Outline each Plasmodium vivax-infected red blood cell.
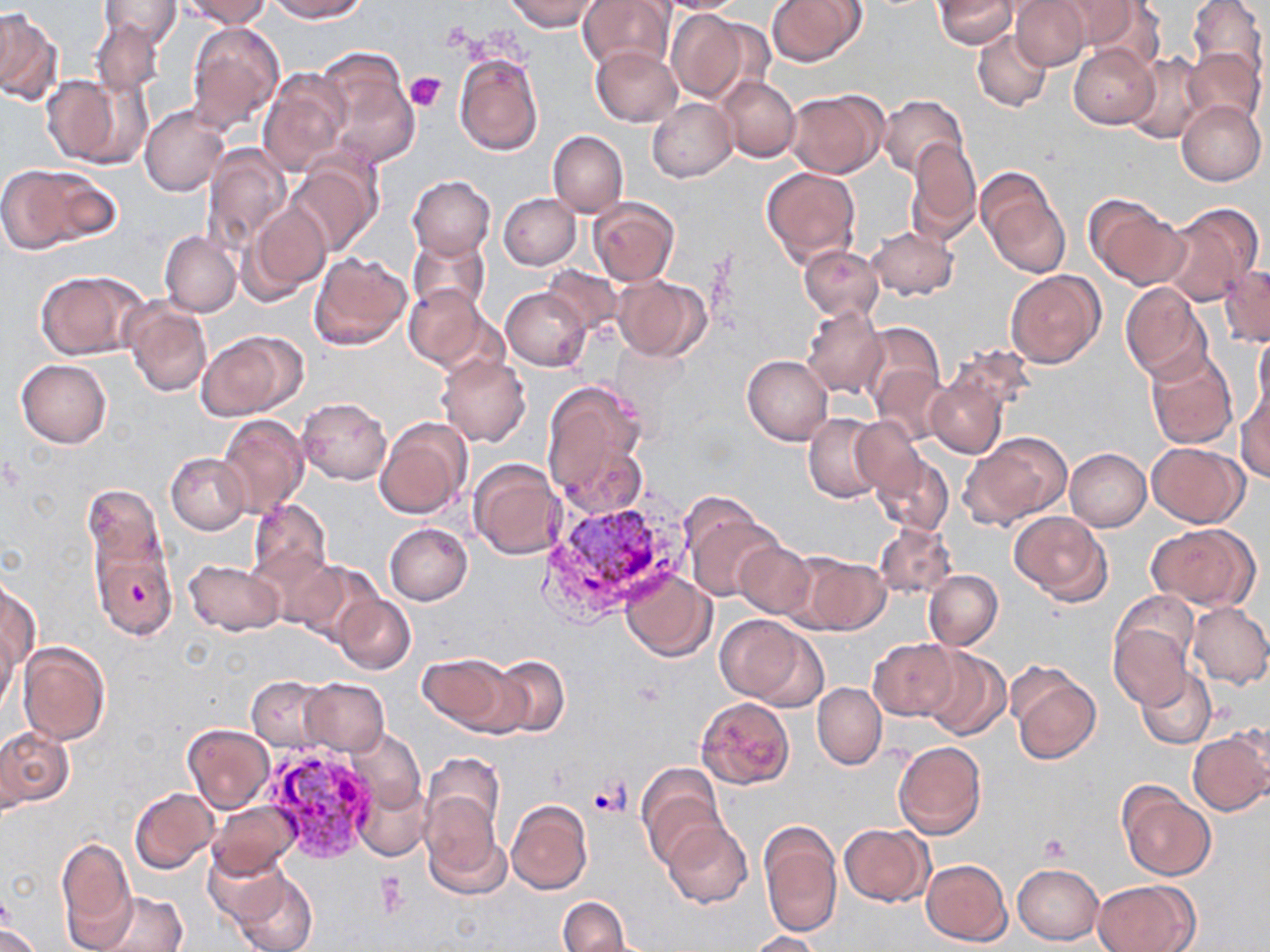

Approximate bounding boxes as (x1, y1, x2, y2) in pixels.
Plasmodium vivax-infected red blood cells: (543, 499, 678, 588), (255, 741, 375, 863).

Uninfected red blood cell locations: (99, 0, 181, 48), (177, 0, 274, 27), (266, 0, 366, 22), (504, 0, 600, 33), (579, 0, 676, 73), (652, 0, 752, 14), (766, 0, 866, 67), (934, 0, 1018, 49), (1010, 0, 1092, 70), (1052, 0, 1151, 54), (1186, 0, 1267, 81), (1019, 2, 1158, 84), (0, 8, 62, 105), (666, 8, 761, 104), (91, 17, 165, 98), (186, 21, 285, 134), (972, 30, 1052, 112), (1069, 43, 1160, 128), (591, 46, 683, 127), (1184, 48, 1265, 128), (454, 51, 544, 156), (1123, 52, 1209, 144), (314, 55, 420, 173), (260, 68, 352, 175), (40, 73, 132, 168), (715, 76, 800, 162), (784, 88, 886, 178), (879, 95, 968, 180), (647, 99, 737, 182), (1176, 100, 1266, 185), (140, 105, 231, 197), (548, 130, 628, 217), (905, 138, 981, 243), (201, 143, 293, 252), (286, 157, 382, 255), (1, 162, 118, 253), (762, 166, 861, 270), (978, 171, 1068, 276), (408, 176, 495, 259), (498, 194, 581, 270), (1086, 195, 1190, 289), (588, 197, 678, 287), (240, 203, 329, 304), (1159, 203, 1263, 304), (868, 227, 958, 299), (160, 232, 241, 317), (408, 232, 491, 316), (800, 246, 883, 321), (308, 250, 412, 351), (1219, 264, 1269, 346), (541, 266, 623, 334), (34, 270, 146, 360), (1006, 270, 1106, 370), (612, 275, 710, 360), (1120, 282, 1212, 382), (403, 284, 490, 371), (501, 287, 591, 370), (122, 300, 212, 398), (802, 304, 886, 399), (860, 321, 944, 412), (1254, 329, 1270, 421), (197, 331, 300, 421), (948, 347, 1034, 423), (1145, 348, 1239, 450), (743, 355, 833, 445), (438, 356, 530, 446), (16, 359, 111, 447), (872, 365, 951, 444), (926, 370, 1009, 459), (541, 379, 650, 512), (1236, 388, 1270, 483), (297, 398, 391, 485), (803, 412, 886, 503), (218, 414, 309, 517), (850, 416, 924, 497), (374, 417, 470, 520), (959, 431, 1072, 530), (1147, 442, 1247, 527), (1064, 448, 1150, 530), (870, 450, 955, 537), (166, 452, 250, 534), (467, 459, 564, 561), (82, 485, 169, 584), (683, 494, 781, 592), (248, 498, 333, 595), (1009, 511, 1110, 602), (873, 522, 956, 598), (384, 523, 474, 605), (1146, 524, 1259, 611), (89, 527, 175, 642), (734, 542, 814, 621), (251, 548, 343, 631), (796, 554, 890, 635), (183, 559, 284, 635), (292, 560, 384, 645), (620, 569, 716, 661), (924, 570, 1002, 650), (1, 578, 39, 674), (1114, 591, 1200, 675), (335, 595, 416, 674), (1188, 602, 1270, 688), (715, 615, 816, 706), (1109, 622, 1192, 710), (0, 628, 18, 715), (868, 639, 958, 720), (17, 642, 110, 745), (918, 646, 1011, 740), (417, 654, 518, 733), (490, 655, 569, 737), (1010, 666, 1101, 764), (1135, 666, 1218, 751), (246, 676, 332, 753), (300, 679, 389, 756), (812, 683, 886, 769), (697, 696, 793, 789), (182, 722, 274, 813), (1189, 727, 1270, 816), (0, 728, 73, 808), (346, 729, 425, 814), (893, 740, 986, 840), (423, 752, 504, 842), (637, 764, 726, 867), (354, 781, 431, 861), (1118, 783, 1216, 882), (130, 787, 220, 874), (421, 796, 505, 895), (506, 799, 592, 894), (208, 801, 299, 879), (662, 820, 753, 909), (759, 820, 842, 938), (839, 823, 934, 906), (55, 838, 136, 946), (202, 847, 293, 926), (921, 860, 1011, 946), (1013, 863, 1103, 945), (230, 866, 318, 952), (1094, 879, 1198, 952), (84, 889, 188, 952), (558, 895, 629, 952), (0, 924, 41, 952), (749, 930, 822, 952). Platelet locations: (404, 72, 445, 111), (1039, 834, 1069, 861), (375, 875, 407, 916). Slide-level diagnosis: Plasmodium vivax. Captured at 1000x magnification. Image is 1270×952 pixels. Optical microscopy. Thin blood film. May-Grünwald-Giemsa stain. Single field of view.